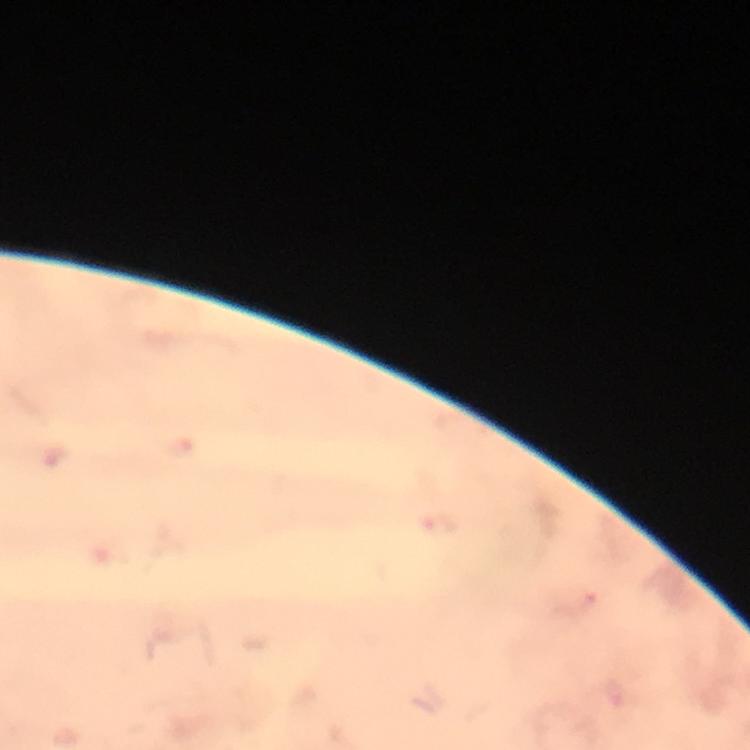

Approximate object centers, in pixels from the top-left corner. Plasmodium parasite locations: (x=440, y=524). Photographed through the microscope with a smartphone camera. From a malaria diagnostic workup. Thick blood smear. Cropped region of a single field of view. Image is 750×750 pixels. Immersion oil was used. Giemsa-stained preparation. At 100x magnification.